Identify the cell.
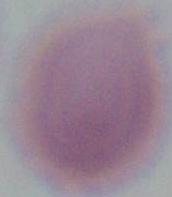
An erythrocyte.

modality = micrograph
magnification = 1000x